Look for parasitized red blood cells.
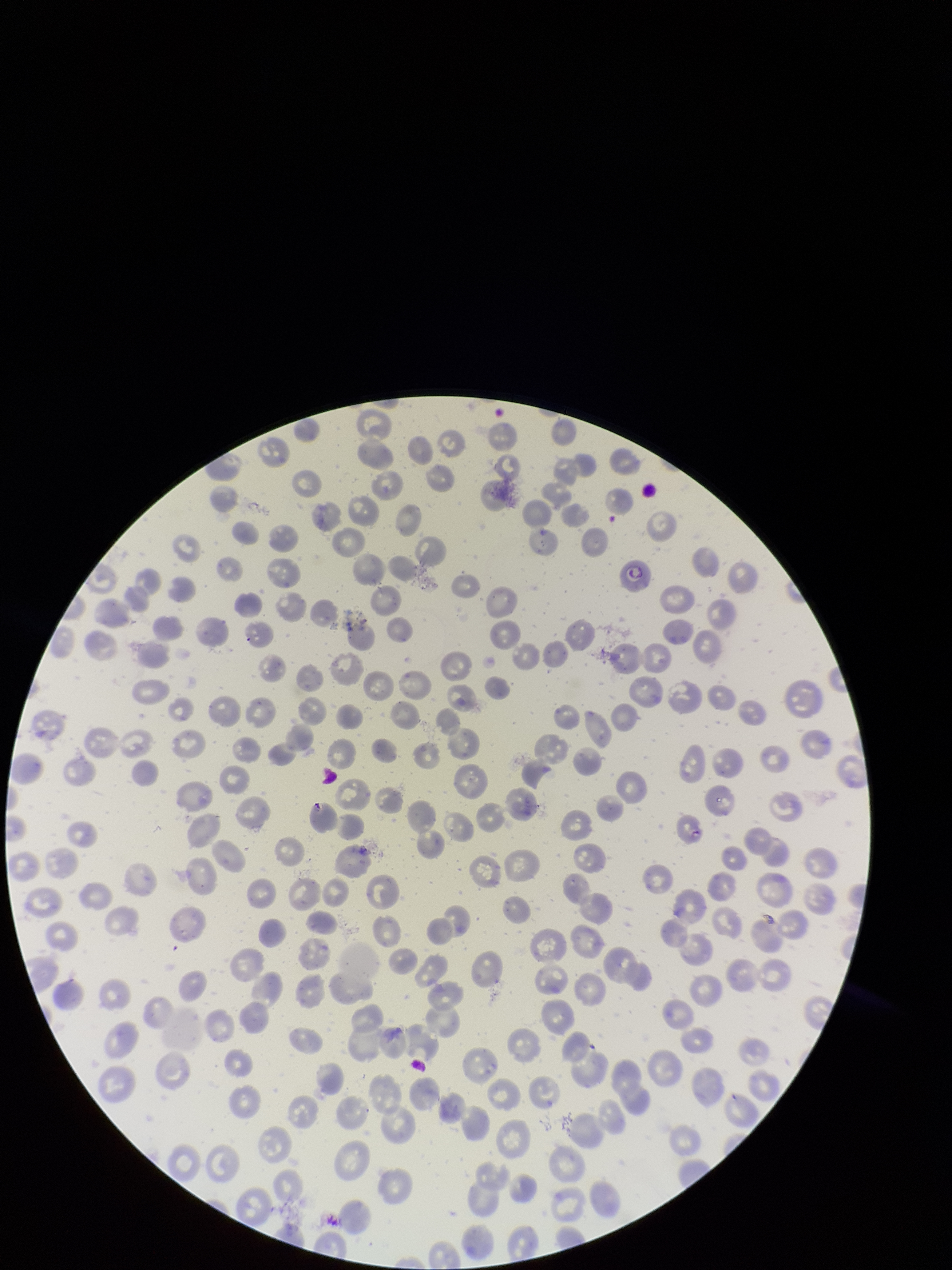

None seen.

{
  "red_blood_cell_count": 227,
  "image_size": "952×1270 pixels",
  "field_of_view": "one from this slide",
  "species_reported_for_this_patient": "Plasmodium falciparum",
  "stain": "Giemsa",
  "preparation": "thin",
  "parasitized_red_blood_cell_count": 0,
  "patient_malaria_status": "infected",
  "capture": "smartphone photograph through the microscope eyepiece"
}